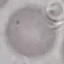
Summary:
  - Result: no malaria parasites detected
  - Stain: Giemsa
  - Capture: smartphone through the microscope eyepiece
  - Preparation: thin blood film
  - Image type: cell patch, automatically extracted from a larger field of view and resized to 64 × 64 pixels